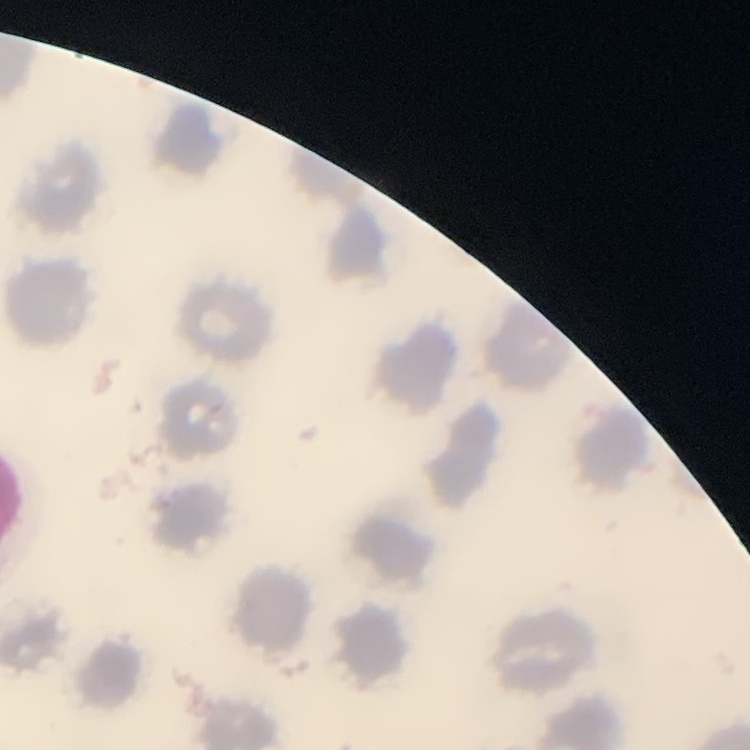
The erythrocytes exhibit no rouleaux formation. Square crop of a larger photomicrograph. Thin blood smear. Field's or Giemsa stain.